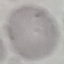

Result: no malaria parasites detected. Giemsa-stained preparation. Automatically extracted cell patch, resized to 64 × 64 pixels. Thin blood film. Photographed with a smartphone camera at the microscope eyepiece.